Comment on the morphology of the erythrocytes.
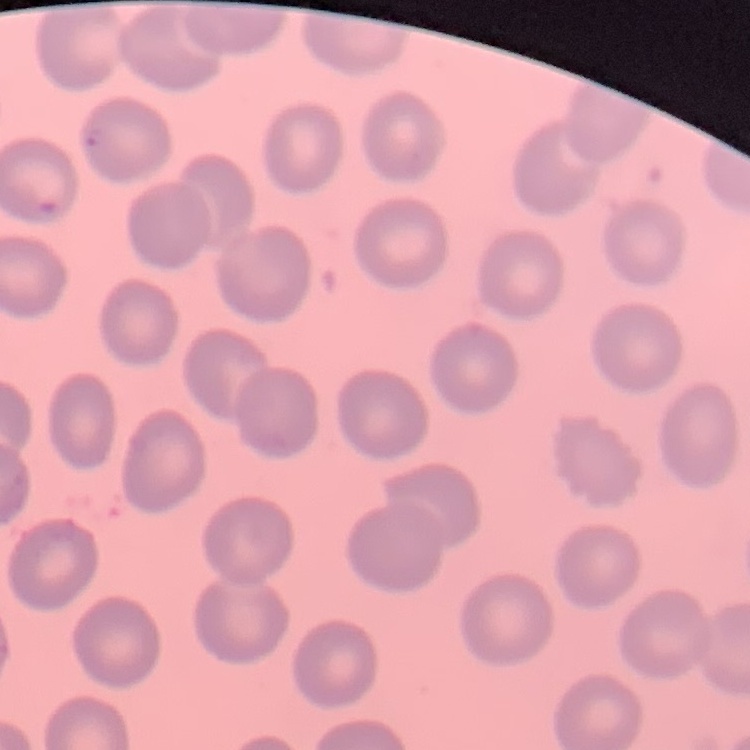

They show no rouleaux formation.

Summary:
  - Stain: Field's or Giemsa
  - Preparation: thin blood film
  - Image type: one tile cut from a larger photomicrograph